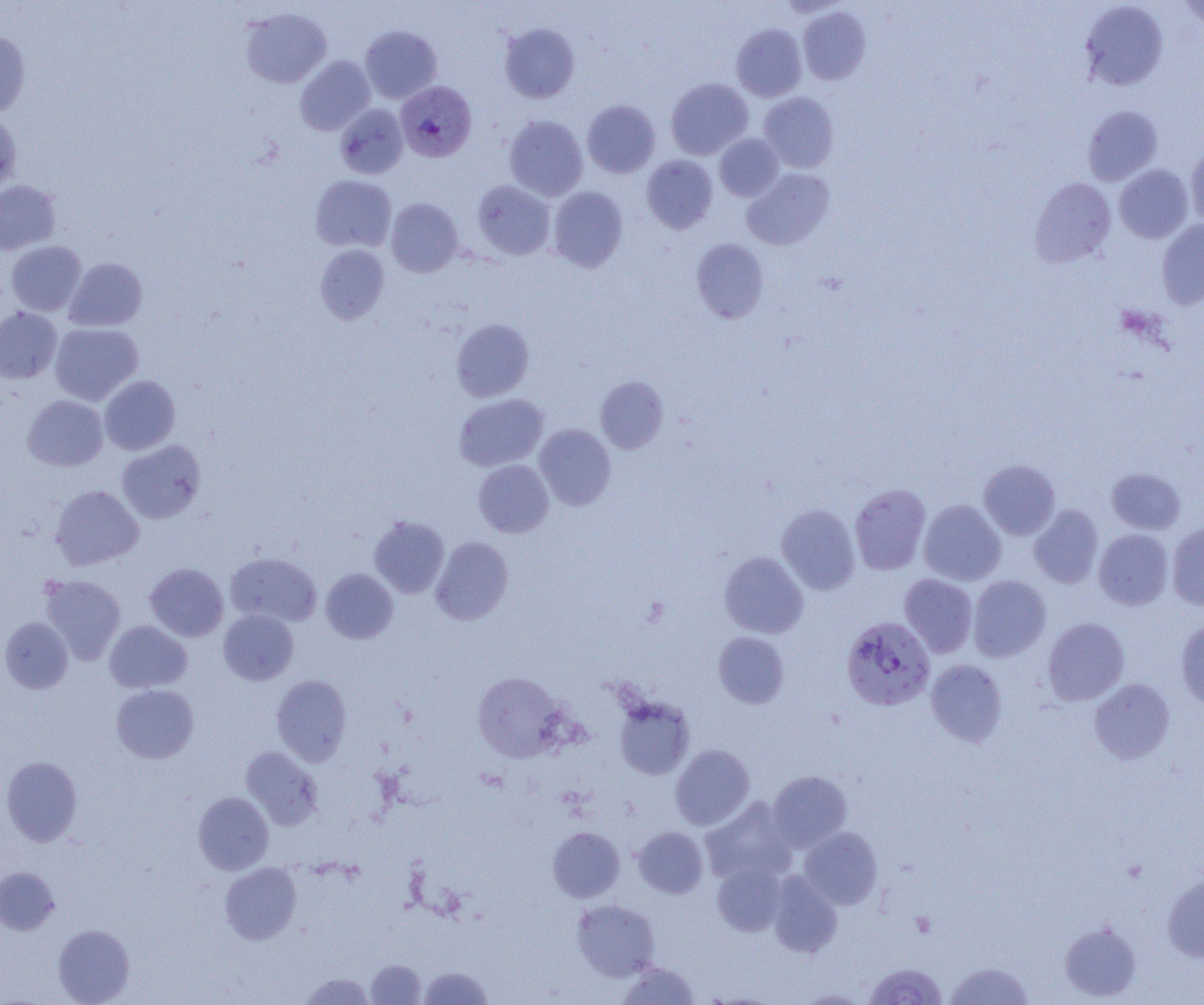

slide-level diagnosis = Plasmodium falciparum
magnification = 1000x
modality = light microscopy
uninfected red blood cell locations = approximate bounding boxes as (x1, y1, x2, y2) in pixels: (1079, 1, 1168, 91), (1176, 1, 1204, 29), (240, 6, 332, 88), (798, 7, 870, 85), (500, 23, 580, 103), (731, 24, 806, 101), (360, 25, 442, 103), (0, 30, 31, 118), (295, 56, 375, 135), (666, 78, 753, 160), (758, 92, 839, 173), (582, 99, 660, 178), (335, 104, 408, 179), (1082, 105, 1162, 186), (0, 112, 21, 192), (504, 115, 588, 201), (715, 133, 783, 201), (1185, 146, 1204, 228), (642, 155, 718, 234), (1114, 164, 1193, 243), (742, 168, 834, 250), (310, 175, 396, 252), (1030, 177, 1116, 267), (0, 179, 60, 254), (472, 180, 555, 259), (548, 186, 628, 271), (386, 198, 463, 277), (1157, 218, 1204, 309), (691, 239, 769, 323), (5, 241, 86, 316), (314, 244, 389, 324), (64, 258, 147, 331), (0, 307, 62, 384), (451, 318, 534, 401), (50, 323, 143, 405), (99, 375, 180, 454), (595, 376, 668, 453), (453, 393, 548, 471), (22, 395, 108, 471), (534, 424, 616, 510), (117, 440, 205, 524), (474, 459, 553, 537), (978, 460, 1060, 539), (1107, 468, 1185, 534), (850, 484, 931, 575), (50, 485, 143, 570), (919, 499, 1006, 585), (776, 504, 860, 595), (1029, 504, 1104, 588), (369, 516, 449, 597), (1167, 522, 1204, 610), (1093, 529, 1174, 610), (431, 536, 513, 625), (225, 552, 322, 627), (719, 552, 809, 638), (145, 563, 228, 641), (321, 569, 398, 644), (39, 574, 125, 664), (899, 574, 978, 658), (968, 575, 1051, 662), (218, 609, 298, 685), (0, 617, 73, 693), (1043, 617, 1129, 705), (1176, 617, 1204, 710), (105, 620, 192, 693), (713, 632, 789, 709), (926, 659, 1007, 747), (472, 672, 567, 762), (272, 675, 352, 765), (1089, 678, 1175, 763), (111, 684, 199, 763), (614, 696, 694, 780), (671, 744, 754, 830), (241, 747, 323, 829), (1, 756, 83, 846), (768, 770, 852, 851), (193, 792, 273, 874), (700, 797, 797, 885), (633, 826, 708, 898), (548, 827, 624, 902), (799, 827, 882, 909), (220, 862, 302, 944), (713, 862, 787, 936), (0, 867, 59, 934), (767, 872, 842, 957), (1162, 874, 1204, 962), (573, 899, 660, 981), (1060, 922, 1142, 1001), (53, 924, 135, 1004), (367, 959, 426, 1004), (618, 961, 699, 1004), (944, 961, 1034, 1004), (419, 966, 493, 1004), (300, 972, 374, 1004), (794, 990, 871, 1004)
Plasmodium falciparum-infected red blood cell locations = approximate bounding boxes as (x1, y1, x2, y2) in pixels: (400, 82, 480, 163), (841, 616, 936, 711), (864, 963, 947, 1004)
preparation = thin blood smear
field of view = single
image size = 1204×1005 pixels